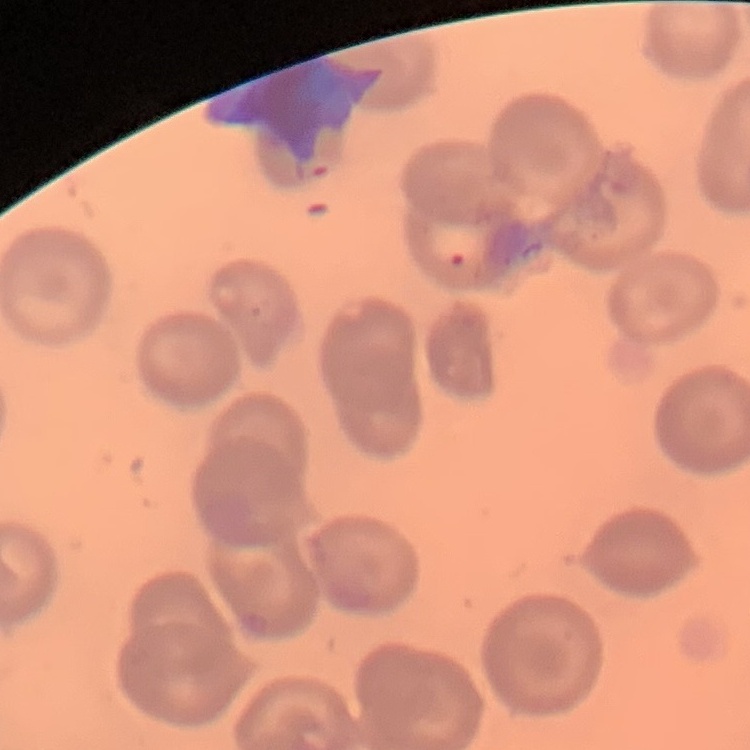

The erythrocytes show no rouleaux formation. Thin blood film. Square crop of a larger photomicrograph. Stained with either Field's or Giemsa.